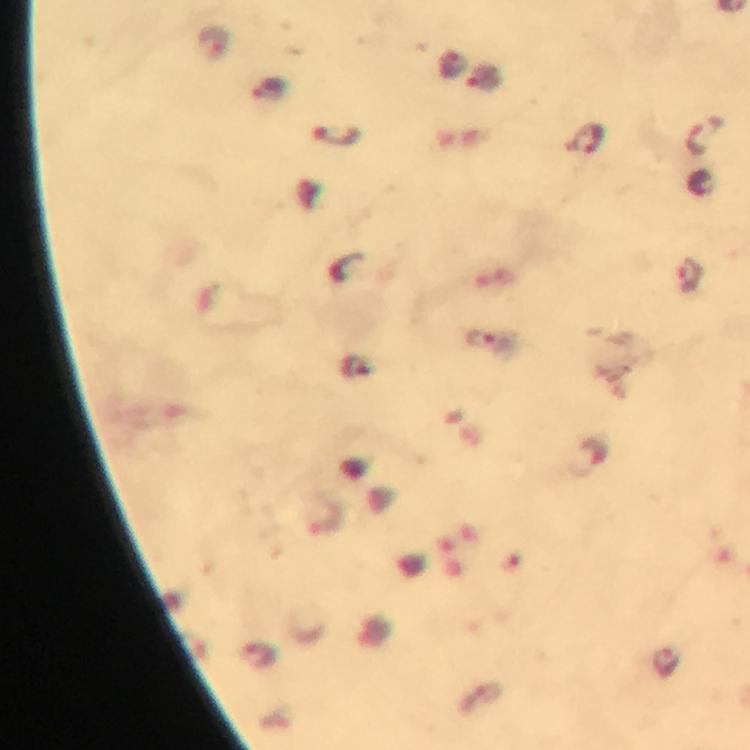
Approximate centers as (x, y) in pixels.
Summary:
  - Malaria parasite locations: (213, 42), (271, 90), (705, 136), (338, 137), (588, 139), (690, 279), (480, 339), (355, 367), (666, 661)
  - Stain: Giemsa
  - Magnification: 100x
  - Context: from a diagnostic examination for malaria
  - Preparation: thick blood film
  - Capture: smartphone photograph through a microscope
  - Image size: 750×750 pixels
  - Cropped from: a single field of view
  - Immersion oil: used